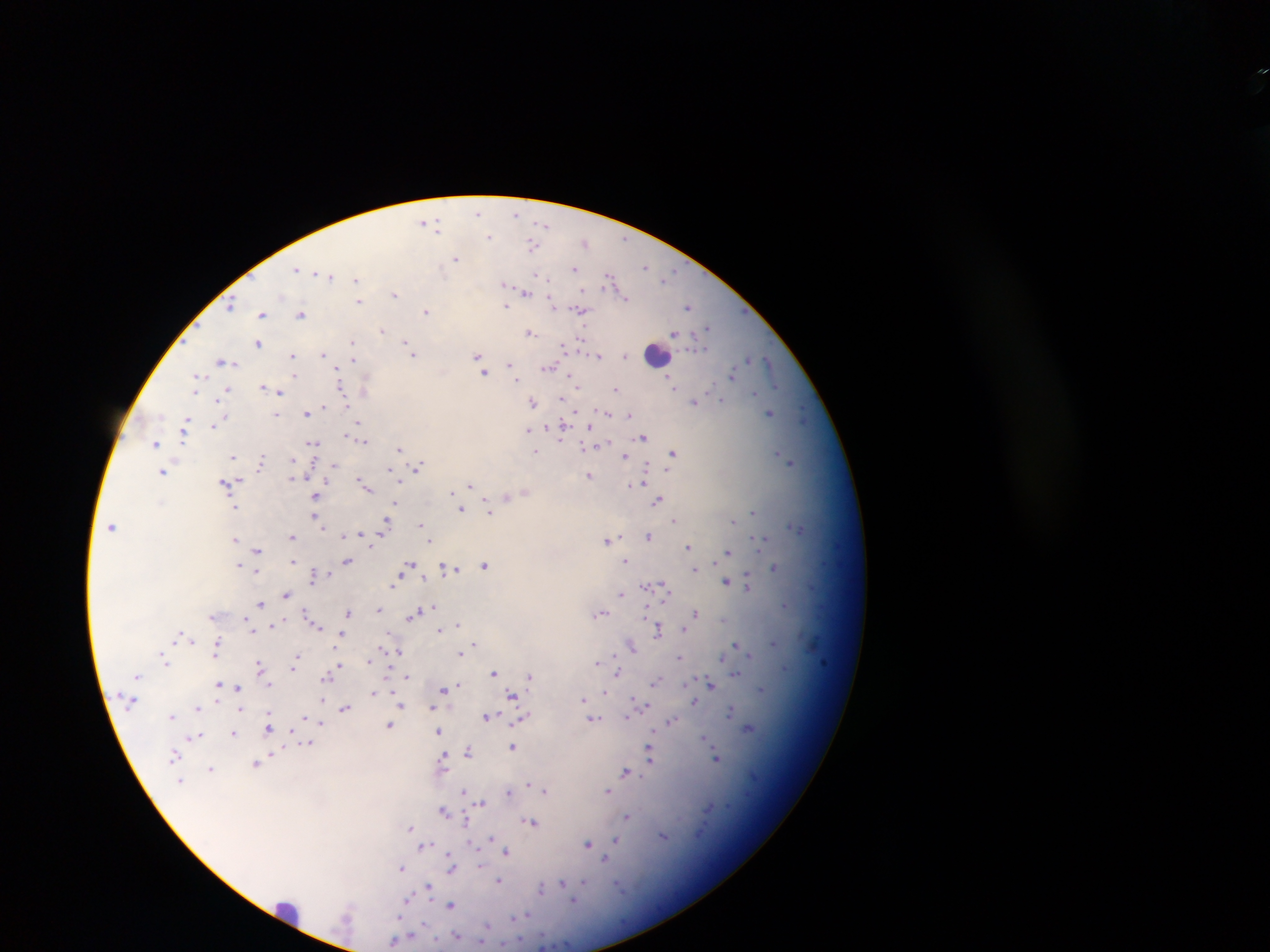

Approximate centers as (x, y) in pixels.
Summary:
  - Leukocyte locations: (656, 355), (289, 911)
  - Malaria parasite locations: (477, 213), (517, 214), (424, 222), (544, 224), (438, 229), (489, 236), (625, 239), (586, 243), (533, 244), (456, 258), (645, 266), (297, 269), (574, 269), (673, 271), (316, 273), (330, 276), (538, 276), (669, 277), (609, 278), (356, 280), (504, 283), (584, 291), (526, 292), (395, 294), (625, 299), (359, 301), (551, 303), (231, 304), (506, 306), (689, 306), (580, 310), (426, 311), (262, 314), (301, 315), (708, 327), (382, 331), (529, 332), (674, 334), (580, 340), (258, 343), (351, 343), (407, 345), (565, 346), (413, 354), (324, 355), (293, 356), (477, 356), (599, 356), (626, 356), (749, 359), (353, 360), (480, 360), (223, 361), (769, 362), (509, 364), (548, 369), (512, 370), (484, 372), (338, 373), (294, 375), (732, 375), (198, 377), (517, 379), (572, 379), (672, 383), (576, 385), (263, 386), (777, 386), (341, 388), (365, 388), (615, 389), (228, 390), (194, 392), (279, 392), (755, 392), (722, 400), (217, 401), (695, 401), (533, 402), (324, 407), (576, 411), (306, 413), (607, 413), (770, 413), (276, 415), (629, 415), (220, 420), (185, 422), (358, 424), (214, 426), (562, 427), (528, 430), (184, 434), (348, 435), (643, 437), (362, 440), (313, 442), (154, 443), (585, 447), (399, 448), (536, 451), (673, 453), (778, 453), (233, 455), (624, 456), (262, 459), (791, 463), (334, 466), (419, 467), (645, 468), (391, 470), (162, 472), (589, 475), (292, 477), (237, 479), (641, 480), (360, 481), (225, 483), (636, 484), (365, 485), (470, 486), (451, 494), (316, 496), (508, 496), (658, 500), (395, 504), (236, 507), (461, 509), (488, 510), (753, 512), (316, 518), (674, 520), (734, 520), (422, 525), (385, 526), (112, 527), (798, 528), (362, 535), (292, 536), (345, 536), (648, 536), (762, 537), (235, 539), (607, 540), (430, 541), (688, 546), (257, 549), (728, 551), (293, 561), (347, 561), (626, 561), (410, 564), (485, 565), (239, 566), (774, 567), (406, 569), (450, 569), (694, 569), (258, 572), (314, 575), (726, 582), (392, 584), (648, 585), (748, 585), (667, 593), (620, 594), (287, 595), (261, 604), (786, 605), (646, 609), (378, 610), (348, 612), (600, 613), (696, 613), (415, 614), (311, 618), (276, 625), (314, 625), (458, 625), (251, 627), (684, 629), (439, 630), (658, 630), (179, 635), (341, 635), (192, 640), (773, 642), (475, 644), (217, 645), (736, 645), (632, 646), (398, 652), (460, 653), (750, 654), (723, 656), (680, 657), (296, 658), (369, 660), (166, 661), (598, 661), (294, 665), (339, 665), (259, 666), (494, 672), (618, 673), (736, 674), (529, 676), (407, 677), (327, 678), (656, 682), (710, 683), (269, 685), (458, 685), (218, 686), (238, 687), (444, 689), (762, 689), (373, 692), (606, 692), (512, 696), (584, 700), (321, 701), (694, 702), (401, 706), (640, 707), (198, 708), (344, 709), (433, 709), (239, 710), (731, 711), (628, 714), (172, 716), (487, 717), (593, 718), (522, 719), (671, 722), (320, 723), (268, 726), (389, 726), (748, 727), (439, 732), (233, 733), (196, 737), (705, 738), (308, 743), (512, 746), (468, 750), (650, 754), (174, 755), (716, 758), (442, 759), (256, 764), (211, 769), (625, 771), (181, 780), (529, 784), (540, 789), (464, 791), (508, 791), (546, 791), (608, 791), (481, 802), (444, 811), (627, 816), (531, 822), (466, 823), (410, 827), (664, 836), (491, 839), (617, 840), (588, 844), (424, 847), (507, 852), (605, 859), (451, 860), (402, 868), (451, 868), (499, 880), (584, 883), (563, 884), (428, 887), (541, 889), (408, 900), (451, 906), (520, 917), (486, 927), (456, 936), (396, 940)
  - Capture: mobile-phone photograph through a microscope
  - Image size: 1270×952 pixels
  - Preparation: thick blood film
  - Field of view: single
  - Country: Ghana